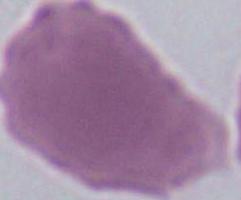
Captured at 1000x magnification. Photomicrograph. A red blood cell is shown.